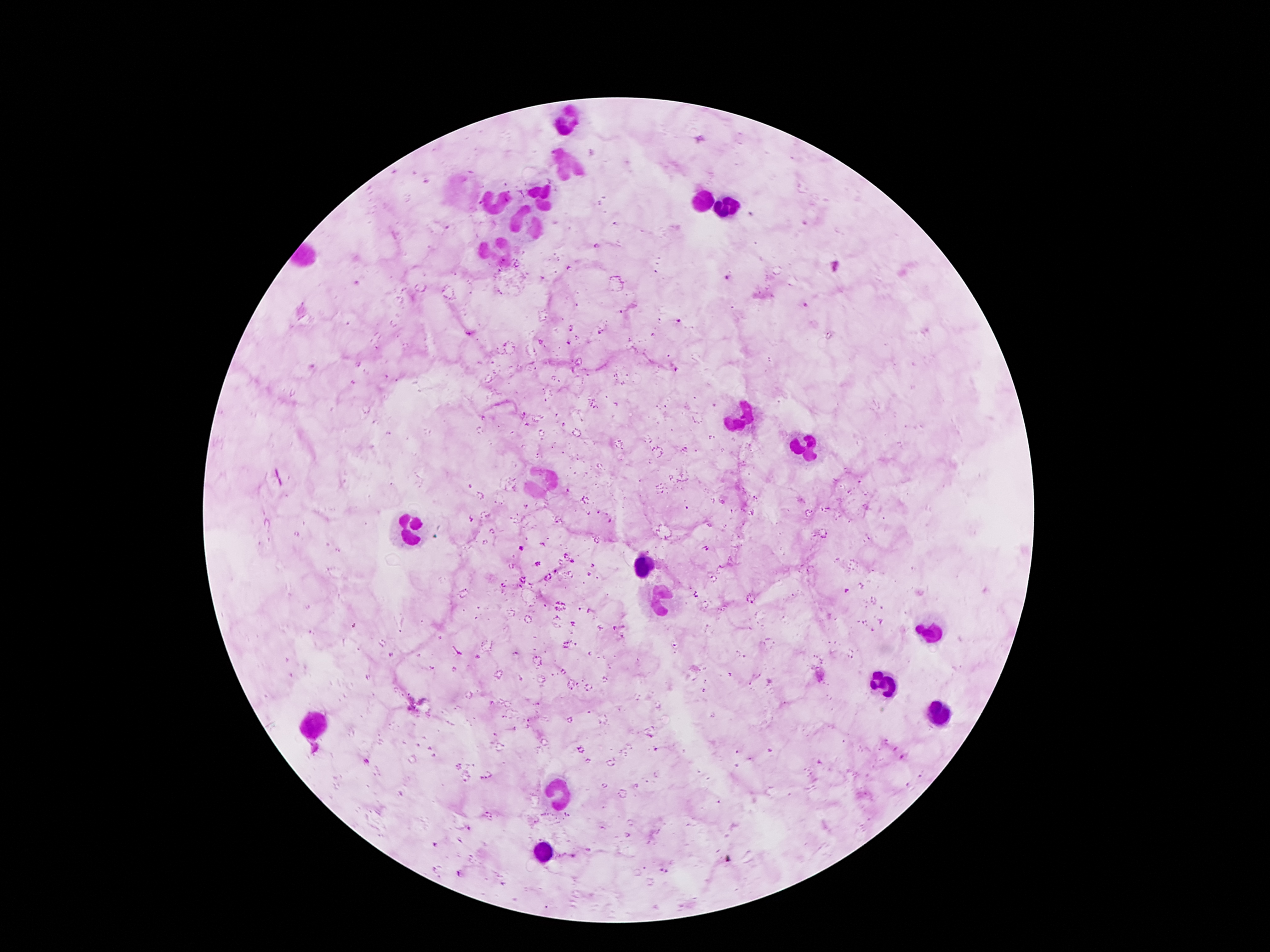

Approximate centers as [x, y] in pixels. Leukocyte locations: [566, 121], [566, 163], [463, 190], [541, 191], [701, 201], [495, 205], [728, 207], [526, 224], [499, 249], [741, 415], [803, 445], [543, 482], [411, 535], [644, 565], [660, 598], [932, 632], [885, 686], [940, 712], [316, 722], [556, 794], [543, 854]. Plasmodium parasite locations: [597, 245], [836, 265], [570, 269], [727, 276], [358, 283], [807, 306], [679, 320], [572, 327], [469, 334], [568, 342], [312, 366], [520, 548], [366, 760], [664, 872], [460, 873]. Patient malaria status: infected with Plasmodium falciparum. Smartphone photograph taken through the microscope eyepiece. 100x magnification. Image is 1270×952 pixels. Giemsa stain. Thick peripheral-blood smear. One field from this slide.